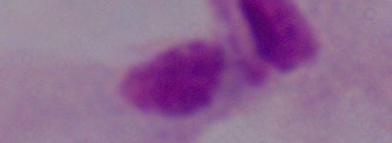

Summary:
  - Identification: trichomonad
  - Magnification: 1000x
  - Modality: photomicrograph